Assess the morphology of the red blood cells.
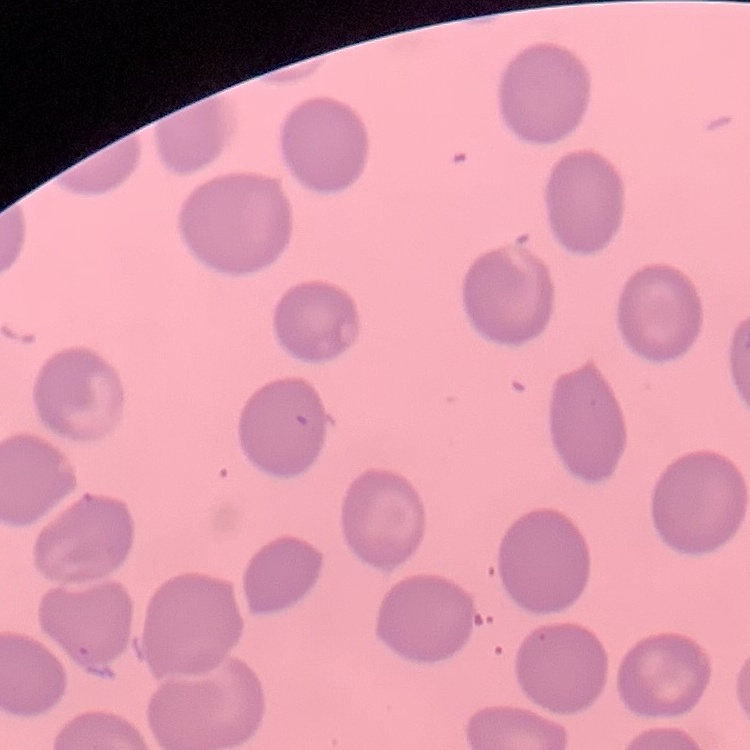

They show no rouleaux formation.

Summary:
  - Image type: one tile cut from a larger photomicrograph
  - Preparation: thin blood film
  - Stain: Field's or Giemsa